Classify this cell by malaria status.
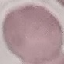

It is uninfected.

Summary:
  - Image type: cell patch, automatically extracted from a larger field of view and resized to 64 × 64 pixels
  - Preparation: thin blood film
  - Capture: smartphone through the microscope eyepiece
  - Stain: Giemsa